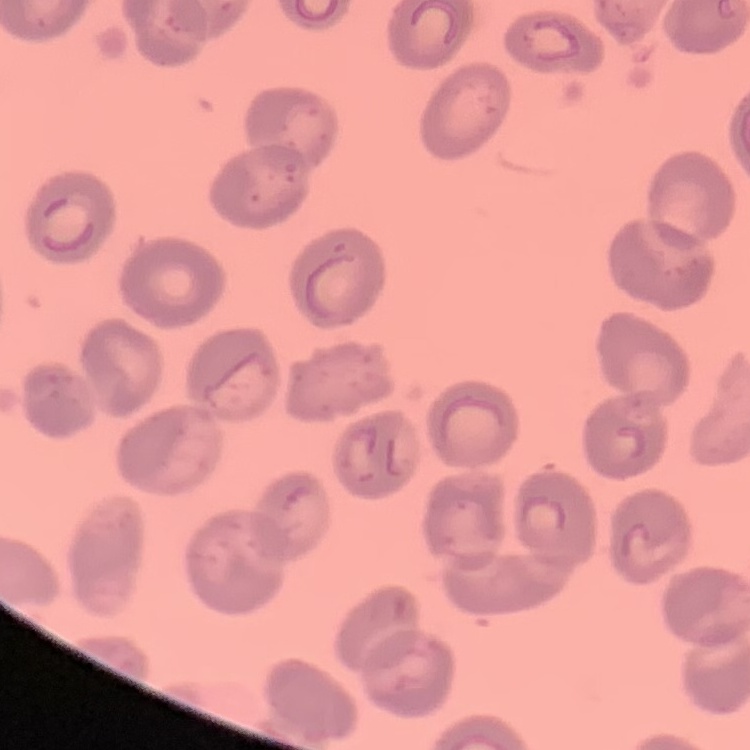
The erythrocytes exhibit no rouleaux formation. Field's or Giemsa stain. Square crop of a larger photomicrograph. Thin peripheral smear.